Assess this cell for malaria.
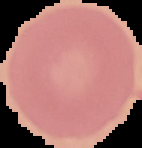
Uninfected.

The area outside the segmented cell region is set to black. Image is 142×148 pixels. From a thin blood smear.